Give the extent of all Plasmodium falciparum-infected red blood cells.
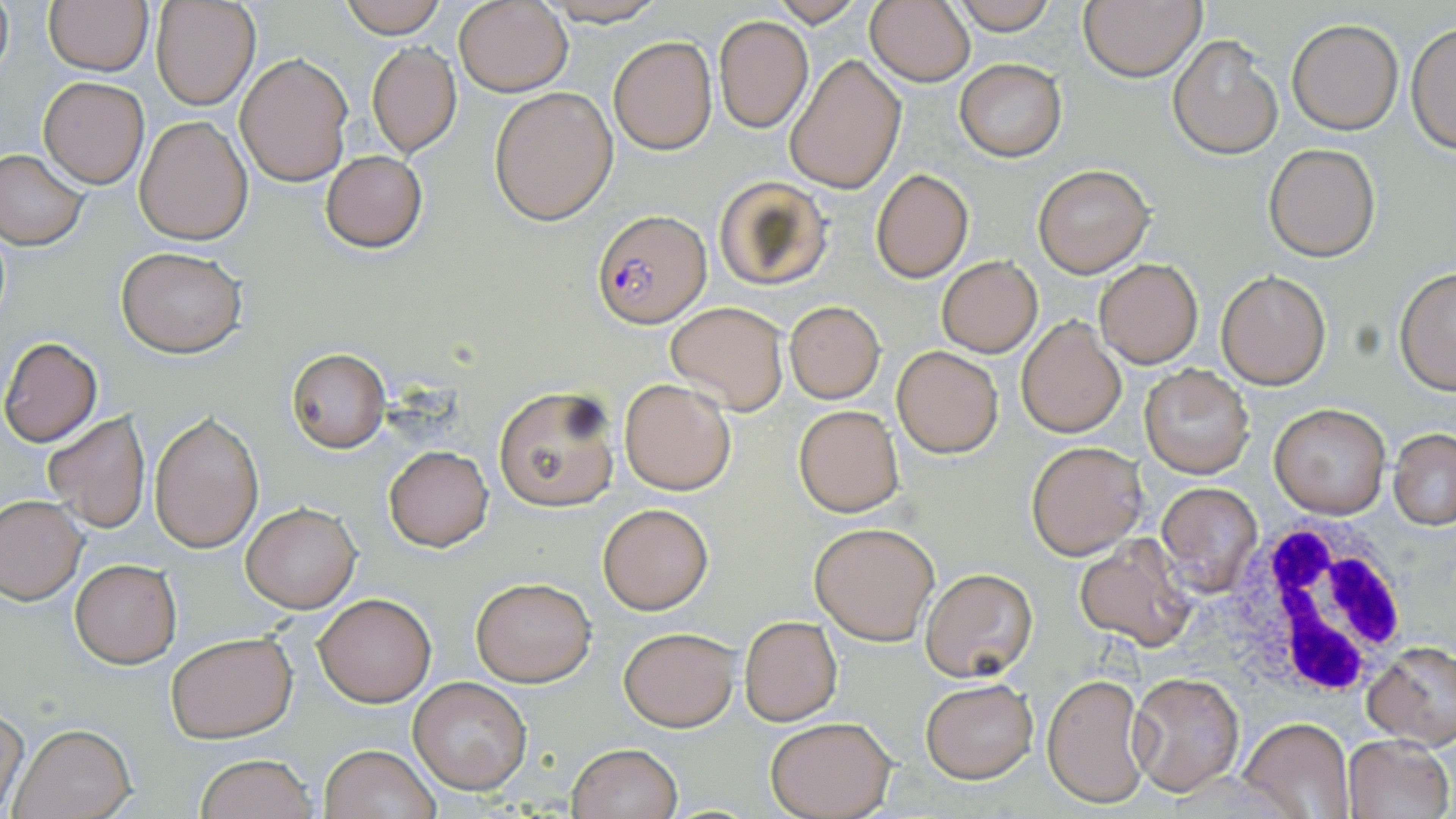
Approximate bounding boxes as [x1, y1, x2, y2] in pixels.
Plasmodium falciparum-infected red blood cells: [593, 213, 713, 330].

Summary:
  - Uninfected red blood cell locations: [337, 0, 448, 36], [541, 0, 673, 26], [769, 0, 864, 26], [865, 0, 976, 87], [953, 0, 1057, 34], [1079, 0, 1205, 81], [42, 1, 152, 78], [150, 1, 259, 109], [455, 1, 572, 96], [713, 15, 814, 134], [1285, 20, 1403, 135], [1408, 23, 1455, 155], [607, 35, 717, 155], [1168, 36, 1282, 160], [366, 43, 462, 158], [235, 53, 353, 186], [786, 55, 905, 192], [953, 58, 1067, 161], [39, 76, 149, 188], [489, 87, 619, 224], [134, 115, 252, 244], [1263, 143, 1380, 262], [0, 148, 89, 249], [320, 150, 428, 253], [1033, 165, 1153, 278], [870, 169, 972, 282], [713, 177, 834, 292], [116, 246, 247, 357], [936, 255, 1043, 357], [1095, 259, 1203, 368], [1394, 267, 1456, 394], [1216, 272, 1331, 389], [666, 301, 788, 416], [784, 301, 884, 403], [1016, 316, 1126, 437], [1, 337, 104, 447], [286, 347, 391, 453], [892, 347, 1003, 457], [1139, 362, 1256, 478], [620, 379, 736, 495], [492, 385, 620, 513], [1270, 401, 1391, 519], [793, 404, 905, 516], [43, 411, 151, 532], [151, 411, 264, 553], [1389, 430, 1456, 529], [1026, 441, 1145, 559], [384, 445, 494, 551], [1155, 482, 1263, 592], [0, 495, 86, 603], [242, 502, 360, 613], [598, 502, 713, 614], [810, 521, 940, 646], [1075, 535, 1196, 651], [71, 558, 181, 668], [918, 567, 1037, 683], [471, 577, 596, 686], [312, 592, 435, 706], [739, 615, 842, 726], [619, 626, 739, 731], [165, 631, 295, 742], [1362, 643, 1456, 749], [1041, 671, 1150, 809], [1129, 672, 1244, 795], [408, 676, 532, 793], [920, 679, 1037, 783], [0, 706, 28, 813], [765, 717, 894, 819], [1239, 717, 1354, 819], [10, 724, 137, 819], [1343, 735, 1455, 818], [566, 743, 683, 819], [320, 744, 438, 819], [194, 753, 319, 819]
  - White blood cell locations: [1225, 521, 1410, 701]
  - Slide-level diagnosis: Plasmodium falciparum
  - Modality: optical microscopy
  - Stain: May-Grünwald-Giemsa
  - Preparation: thin blood smear
  - Image size: 1456×819 pixels
  - Magnification: 1000x
  - Field of view: one of a larger specimen